State which parasite is depicted.
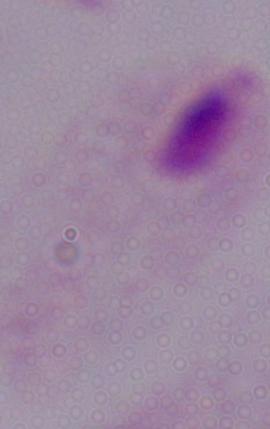

A trichomonad.

magnification = 1000x
modality = photomicrograph